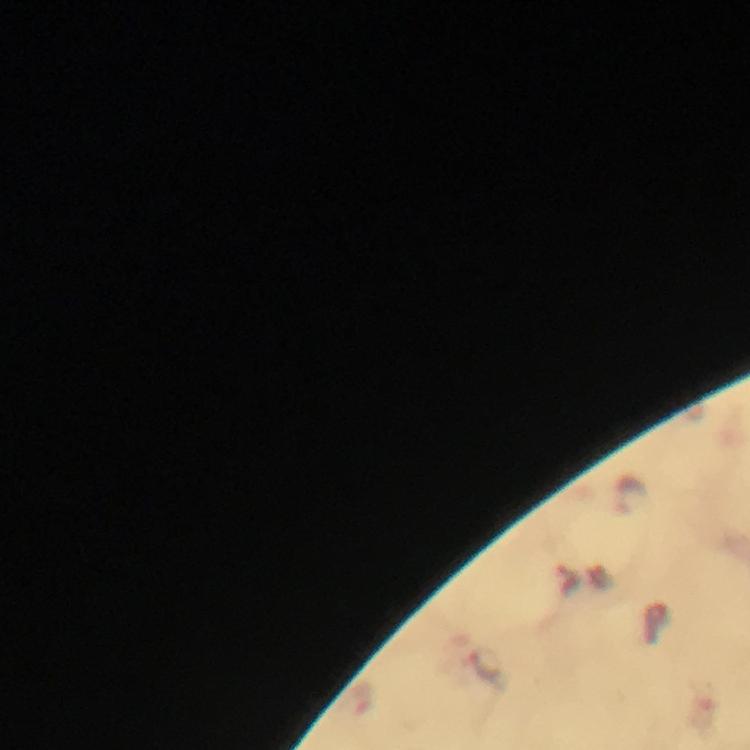 Approximate centers as {x, y} in pixels. Malaria parasite locations: {485, 665}. Image is 750×750 pixels. Thick blood film. Cropped region of a single field of view. Smartphone photograph taken through a microscope. Giemsa-stained preparation. Immersion oil was used. From a malaria diagnostic workup. 100x magnification.